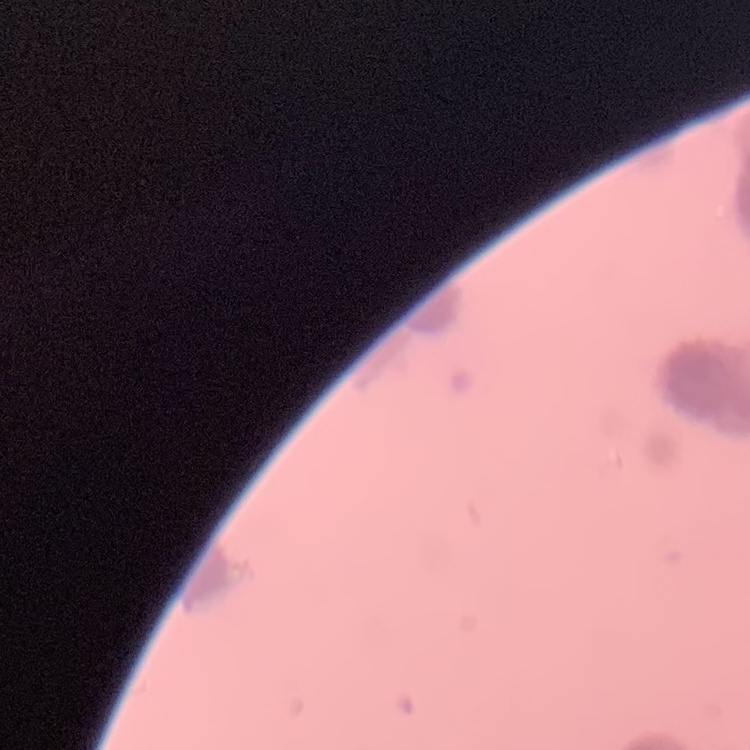

erythrocyte morphology = rouleaux formation
preparation = thin blood smear
stain = Field's or Giemsa
image type = square crop of a larger photomicrograph